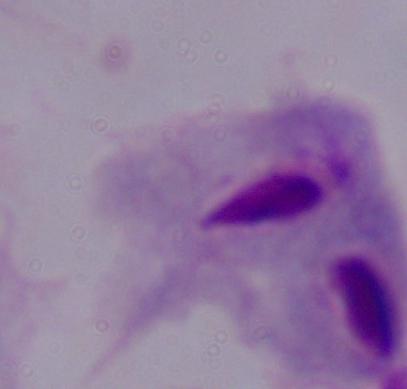

Summary:
  - Modality: micrograph
  - Magnification: 1000x
  - Identification: trichomonad